Classify this cell by malaria status.
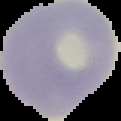
It is uninfected.

Segmented cell region on a black background. Image is 121×121 pixels. From a thin blood smear.